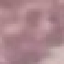
Result: no malaria parasites seen. Automatically extracted cell patch, resized to 64 × 64 pixels. Thin blood smear. Photographed with a smartphone camera at the microscope eyepiece. Giemsa-stained preparation.